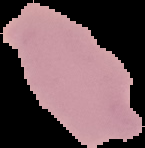

malaria_status: uninfected
image_type: cell region segmented out of the field of view; surrounding area masked to black
preparation: thin blood film
image_size: 145×148 pixels